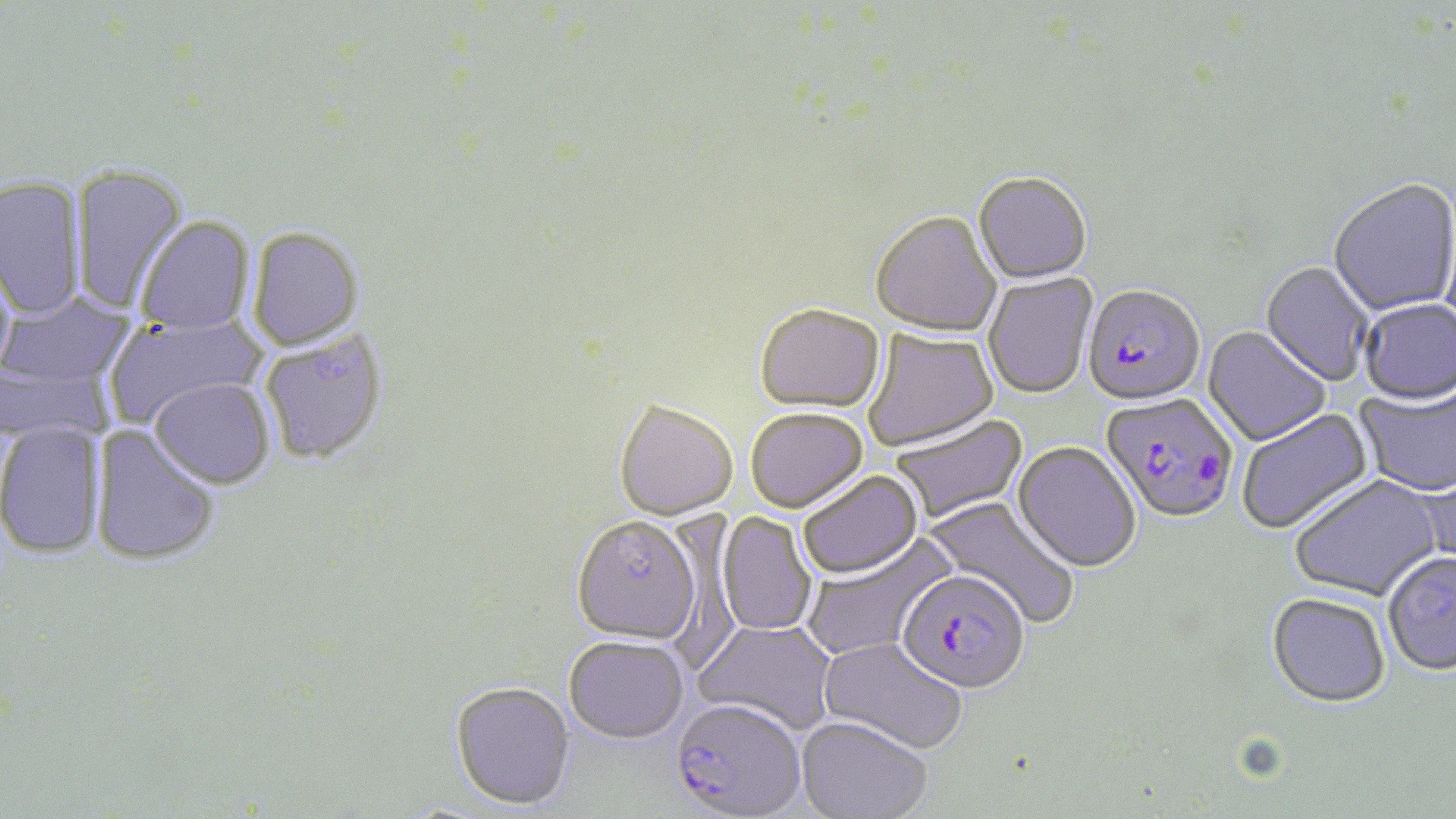
Summary:
  - Coordinate format: approximate bounding boxes as named x1/y1/x2/y2 corners in pixels
  - Uninfected red blood cell locations: (x1=71, y1=162, x2=188, y2=314), (x1=973, y1=174, x2=1092, y2=286), (x1=0, y1=175, x2=86, y2=321), (x1=1328, y1=180, x2=1456, y2=318), (x1=871, y1=213, x2=1001, y2=339), (x1=135, y1=217, x2=255, y2=337), (x1=247, y1=227, x2=365, y2=352), (x1=0, y1=248, x2=17, y2=379), (x1=1259, y1=262, x2=1374, y2=387), (x1=983, y1=272, x2=1097, y2=401), (x1=0, y1=292, x2=137, y2=388), (x1=1359, y1=300, x2=1456, y2=407), (x1=755, y1=307, x2=885, y2=417), (x1=102, y1=314, x2=266, y2=428), (x1=1202, y1=326, x2=1332, y2=448), (x1=862, y1=328, x2=999, y2=453), (x1=259, y1=330, x2=388, y2=466), (x1=0, y1=359, x2=113, y2=446), (x1=150, y1=377, x2=275, y2=488), (x1=1354, y1=384, x2=1456, y2=498), (x1=614, y1=403, x2=737, y2=523), (x1=1238, y1=407, x2=1375, y2=537), (x1=745, y1=411, x2=868, y2=516), (x1=889, y1=415, x2=1029, y2=525), (x1=0, y1=421, x2=106, y2=559), (x1=91, y1=424, x2=221, y2=567), (x1=1011, y1=442, x2=1141, y2=574), (x1=1416, y1=463, x2=1456, y2=577), (x1=799, y1=472, x2=923, y2=581), (x1=1289, y1=476, x2=1444, y2=603), (x1=923, y1=495, x2=1080, y2=627), (x1=717, y1=512, x2=817, y2=637), (x1=571, y1=518, x2=701, y2=648), (x1=801, y1=535, x2=956, y2=660), (x1=1383, y1=553, x2=1456, y2=678), (x1=1267, y1=595, x2=1390, y2=710), (x1=692, y1=619, x2=838, y2=735), (x1=818, y1=638, x2=967, y2=756), (x1=564, y1=639, x2=689, y2=748), (x1=450, y1=684, x2=575, y2=813), (x1=795, y1=719, x2=931, y2=819)
  - Plasmodium falciparum-infected red blood cell locations: (x1=1082, y1=288, x2=1205, y2=409), (x1=1100, y1=393, x2=1239, y2=526), (x1=896, y1=574, x2=1029, y2=698), (x1=669, y1=702, x2=806, y2=819)
  - Slide-level diagnosis: Plasmodium falciparum
  - Stain: May-Grünwald-Giemsa
  - Preparation: thin blood film
  - Image size: 1456×819 pixels
  - Modality: light microscopy
  - Field of view: one of a larger specimen
  - Magnification: 1000x